Name the parasite shown.
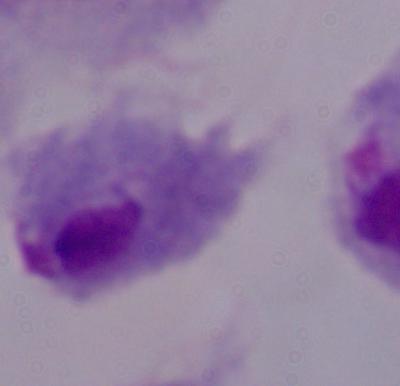

This is a trichomonad.

Photomicrograph. Captured at 1000x magnification.